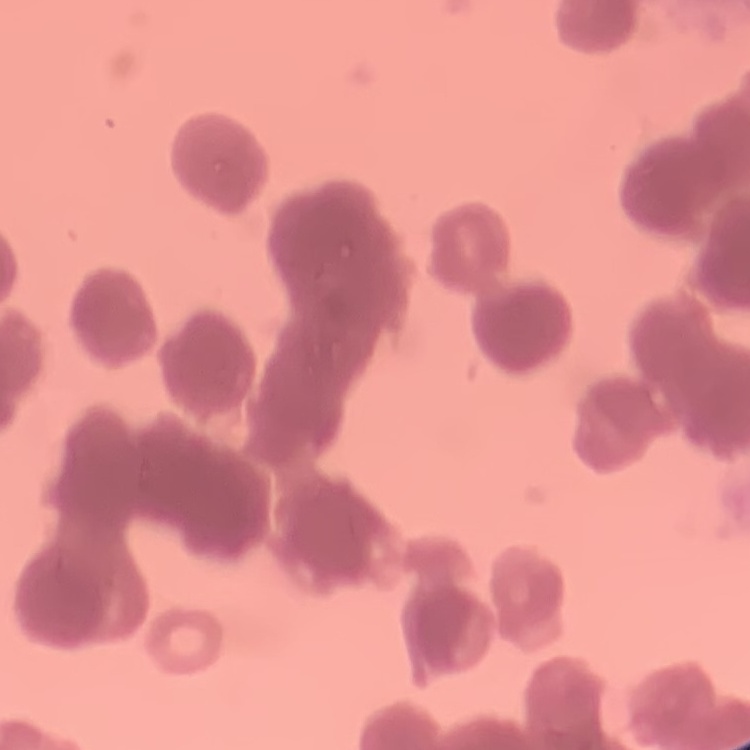

The erythrocytes show rouleaux formation. Stained with either Field's or Giemsa. One tile cut from a larger photomicrograph. Thin peripheral smear.